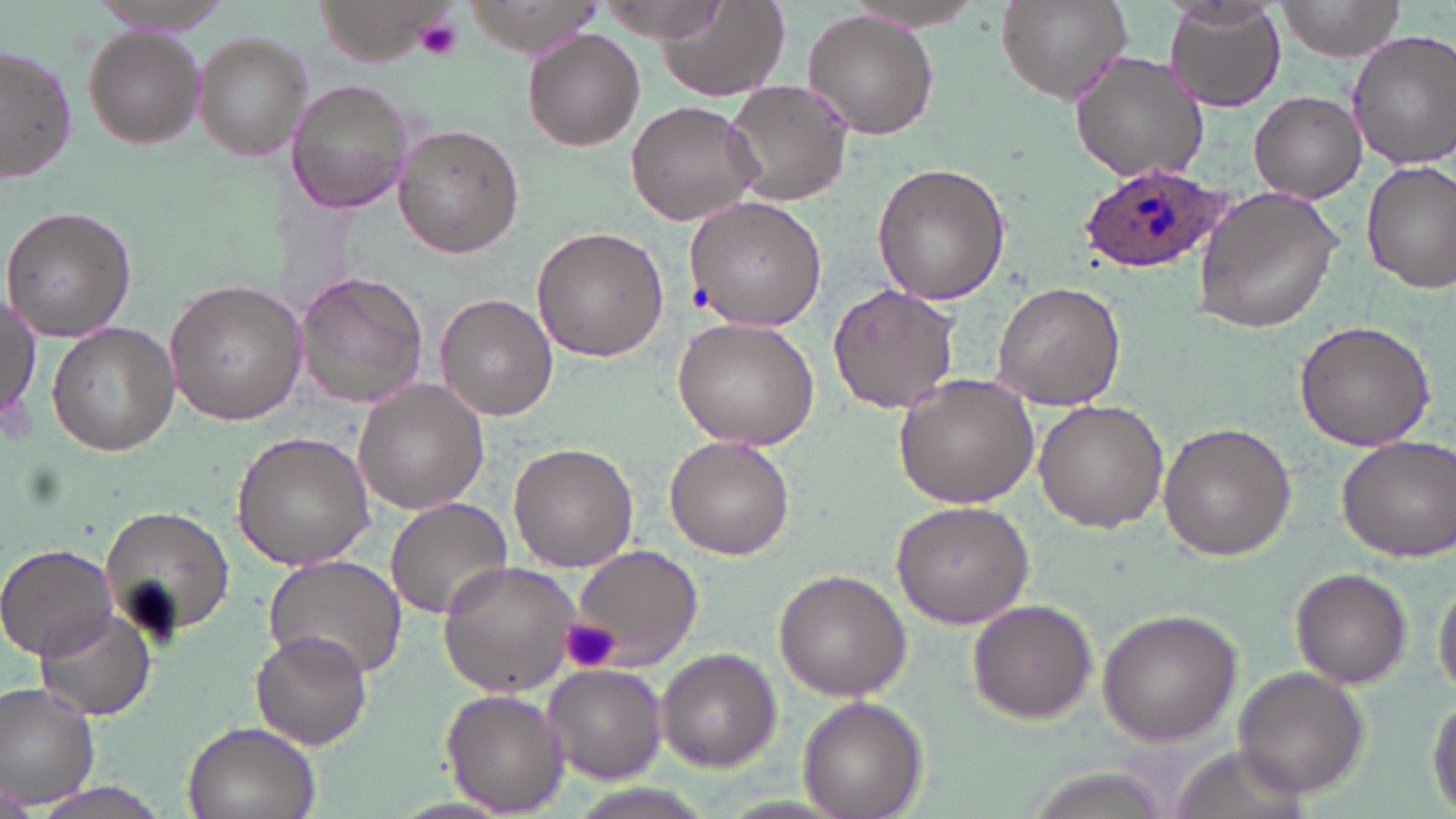
slide-level diagnosis = Plasmodium ovale
magnification = 1000x
image size = 1456×819 pixels
preparation = thin blood film
Plasmodium ovale-infected red blood cell locations = approximate bounding boxes as (x1,y1)-(x2,y2) corner pairs in pixels: (1077,161)-(1224,271)
field of view = single
platelet locations = approximate bounding boxes as (x1,y1)-(x2,y2) corner pairs in pixels: (416,18)-(463,61), (558,617)-(621,674)
uninfected red blood cell locations = approximate bounding boxes as (x1,y1)-(x2,y2) corner pairs in pixels: (88,0)-(244,34), (652,0)-(793,101), (996,0)-(1135,106), (1276,0)-(1407,61), (592,2)-(732,43), (1163,2)-(1287,112), (803,11)-(939,140), (83,27)-(205,149), (522,28)-(648,151), (195,30)-(312,164), (1347,30)-(1456,171), (0,47)-(77,184), (1068,48)-(1212,184), (285,78)-(418,214), (724,80)-(853,208), (1249,89)-(1365,203), (624,100)-(764,227), (393,124)-(525,259), (1361,160)-(1456,293), (871,162)-(1010,305), (1191,186)-(1345,334), (684,196)-(829,329), (1,205)-(135,341), (531,226)-(668,362), (293,270)-(429,410), (163,277)-(306,429), (989,281)-(1127,411), (828,282)-(962,416), (2,290)-(40,432), (434,293)-(558,422), (673,318)-(820,450), (1294,319)-(1436,453), (47,320)-(178,456), (891,374)-(1040,509), (354,381)-(490,517), (1033,400)-(1170,534), (1158,423)-(1296,561), (231,431)-(375,572), (664,435)-(795,560), (1336,436)-(1456,562), (508,443)-(638,572), (384,497)-(514,619), (888,500)-(1035,629), (99,502)-(236,648), (0,543)-(121,660), (570,545)-(705,671), (263,553)-(408,685), (437,561)-(585,694), (775,569)-(913,699), (1292,569)-(1413,689), (1432,572)-(1456,705), (966,599)-(1098,723), (38,607)-(155,721), (1098,608)-(1243,745), (251,631)-(374,751), (656,650)-(780,770), (542,664)-(666,783), (1233,666)-(1368,797), (0,684)-(102,809), (440,688)-(568,815), (1427,689)-(1456,817), (797,696)-(929,819), (177,720)-(319,819), (0,779)-(35,815), (25,780)-(174,819)
modality = optical microscopy
stain = May-Grünwald-Giemsa